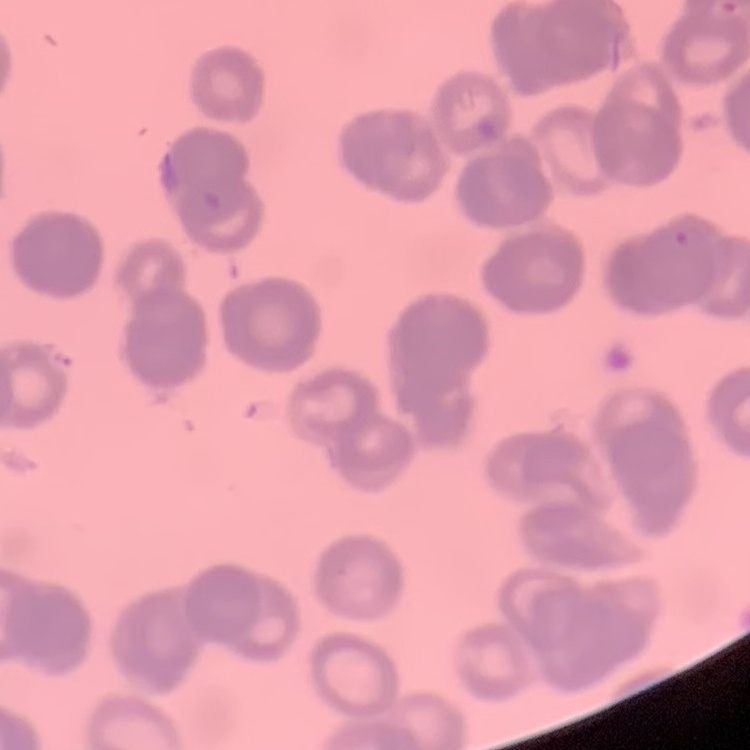
erythrocyte_morphology: rouleaux formation
image_type: square crop of a larger photomicrograph
stain: Field's or Giemsa
preparation: thin peripheral smear